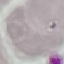

Summary:
  - Malaria status: uninfected
  - Capture: smartphone camera at the microscope eyepiece
  - Image type: cell patch, automatically extracted from a larger field of view and resized to 64 × 64 pixels
  - Stain: Giemsa
  - Preparation: thin smear